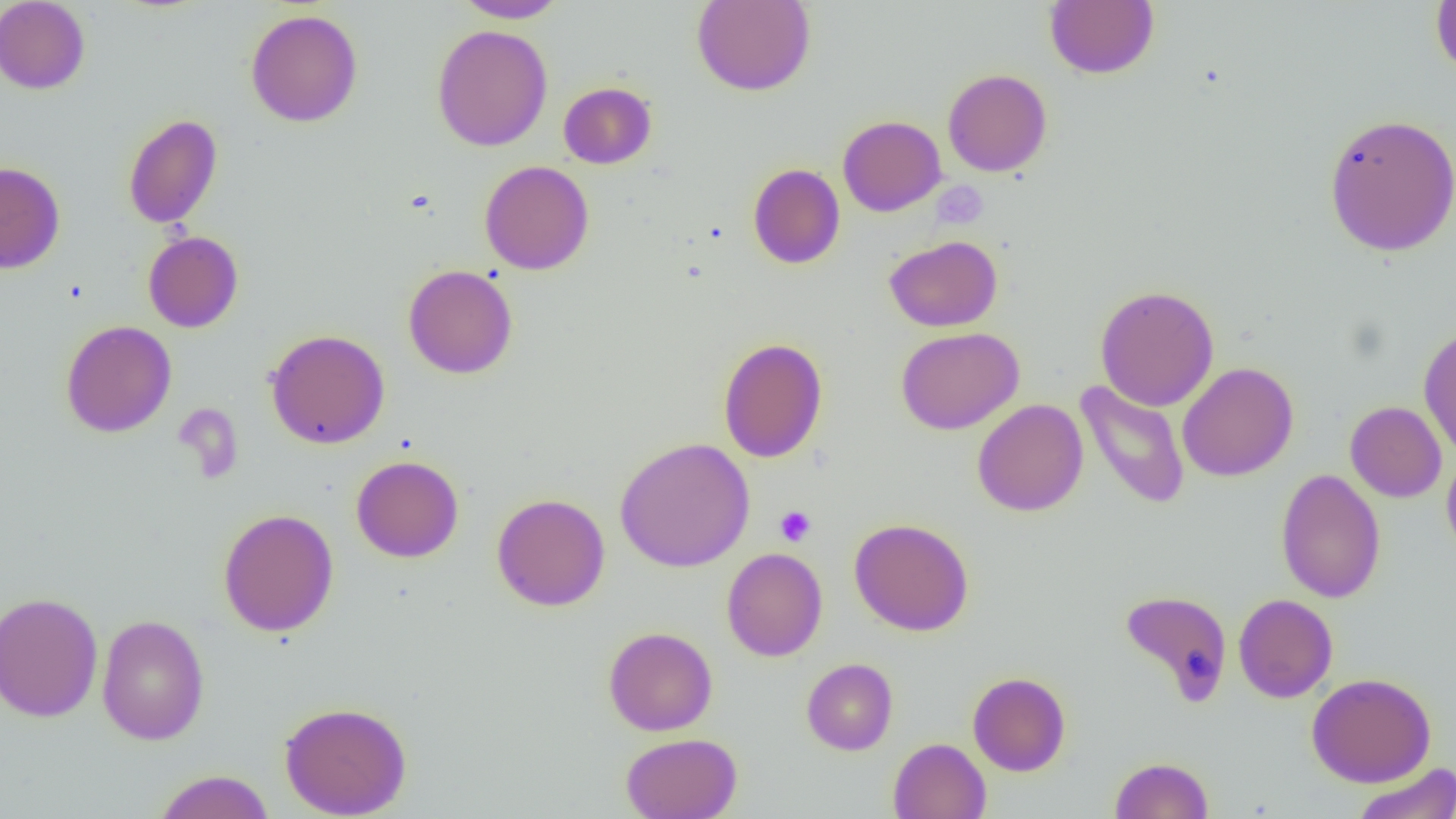

slide_level_diagnosis: negative for blood parasites
preparation: thin blood film
image_size: 1456×819 pixels
modality: light microscopy
uninfected_red_blood_cell_locations: 'approximate bounding boxes as (x1,y1)-(x2,y2) corner pairs in pixels: (454,0)-(568,23), (691,0)-(816,96), (1045,0)-(1159,79), (1431,0)-(1456,79), (0,1)-(90,94), (245,9)-(363,127), (431,24)-(553,151), (943,68)-(1052,177), (559,81)-(656,169), (1323,113)-(1456,257), (122,114)-(222,228), (838,115)-(946,217), (479,161)-(594,275), (0,162)-(65,273), (747,163)-(845,269), (143,231)-(244,333), (884,235)-(1003,332), (403,264)-(518,379), (1095,285)-(1219,411), (61,320)-(177,437), (1418,325)-(1456,458), (896,327)-(1025,435), (265,329)-(390,450), (718,337)-(828,463), (1177,362)-(1298,481), (1076,380)-(1190,510), (972,398)-(1088,516), (1345,401)-(1447,503), (615,437)-(755,573), (1441,451)-(1456,563), (351,456)-(464,562), (1276,468)-(1386,603), (492,493)-(610,611), (218,508)-(339,637), (849,518)-(974,636), (721,547)-(828,662), (1119,589)-(1233,706), (0,591)-(103,722), (1233,594)-(1338,703), (97,614)-(210,745), (603,626)-(718,735), (802,658)-(898,755), (967,671)-(1071,776), (1306,672)-(1436,788), (279,701)-(412,818), (621,732)-(742,819), (888,738)-(991,819), (1110,757)-(1214,819), (1352,763)-(1456,819), (153,769)-(274,819)'
magnification: 1000x
field_of_view: one of a larger specimen
platelet_locations: 'approximate bounding boxes as (x1,y1)-(x2,y2) corner pairs in pixels: (775,506)-(816,546)'